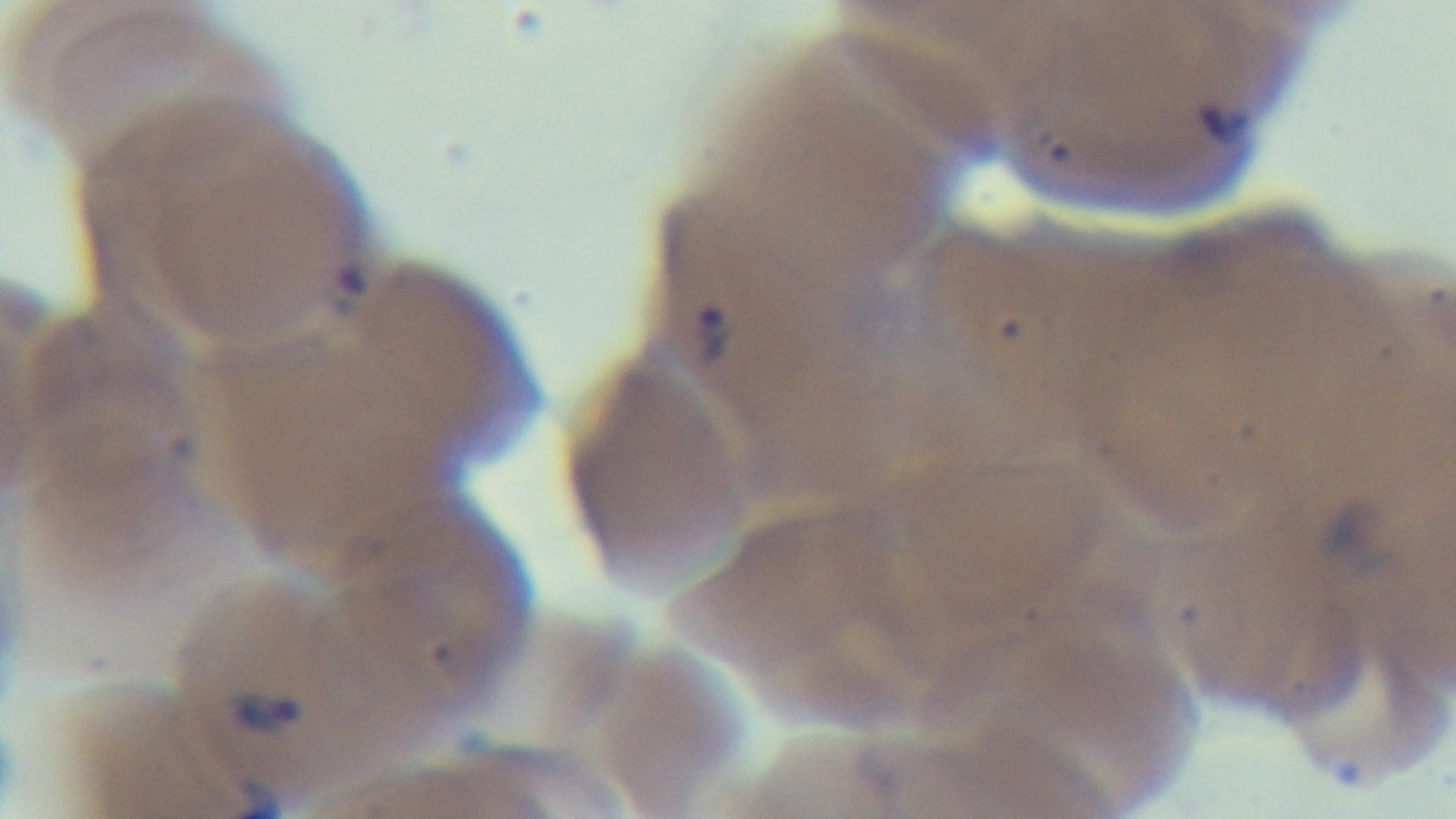

Malaria status: positive. One field from the slide. Mounted 4K digital camera. Preparation: thin. Oil-immersion objective, 100x. Photomicrograph. Giemsa stain.